Locate every uninfected red blood cell.
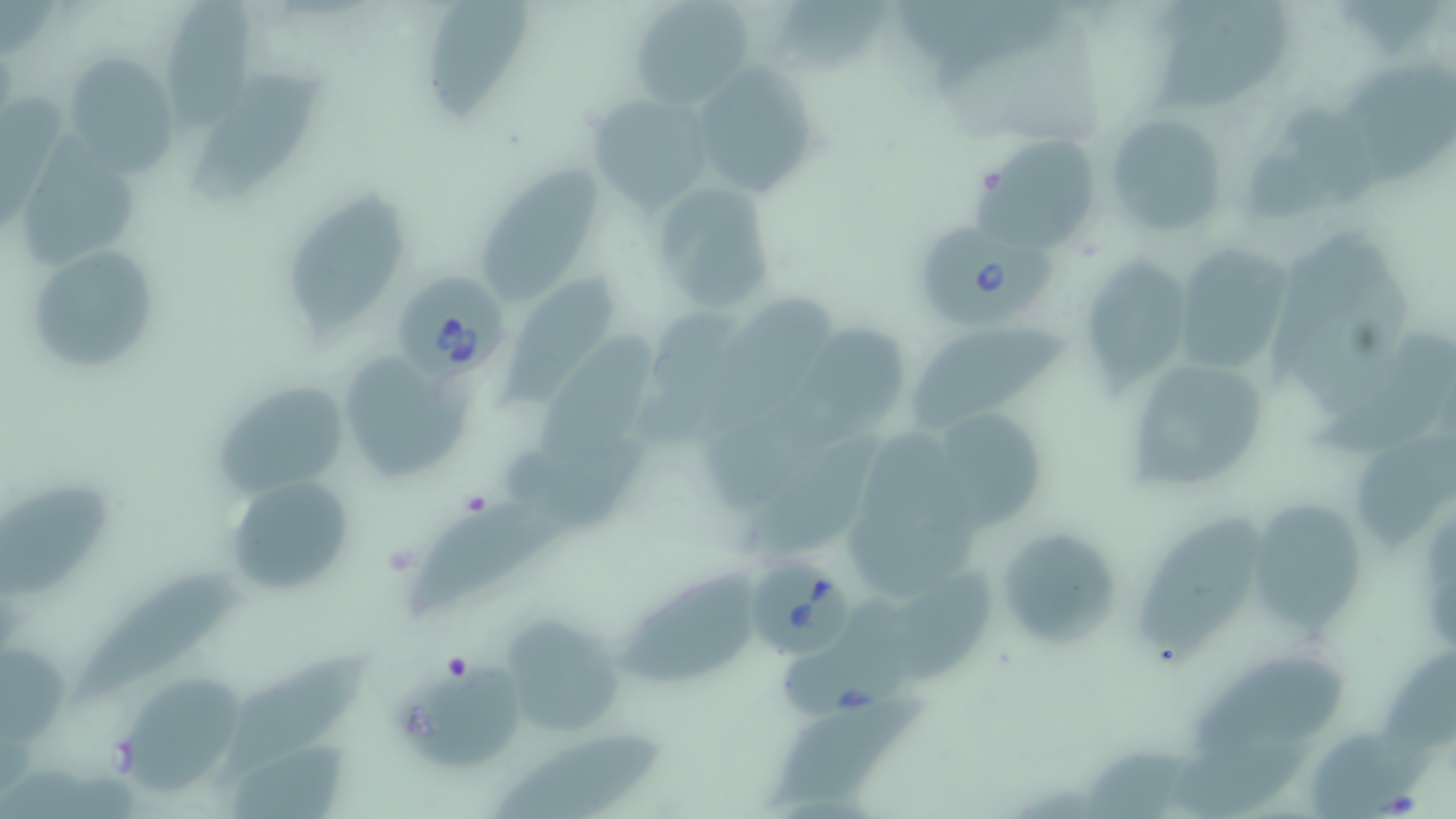
Approximate bounding boxes as (x1,y1)-(x2,y2) corner pairs in pixels.
Uninfected red blood cells: (167,0)-(255,130), (419,0)-(531,131), (627,0)-(756,108), (896,0)-(1066,78), (1160,5)-(1295,117), (63,55)-(180,174), (192,63)-(329,198), (690,64)-(814,197), (587,94)-(713,211), (1248,108)-(1378,225), (1103,112)-(1230,236), (26,132)-(144,267), (972,137)-(1096,241), (482,149)-(603,304), (647,179)-(776,318), (284,182)-(415,343), (22,242)-(161,375), (1180,249)-(1290,371), (1077,256)-(1193,393), (502,267)-(615,406), (701,296)-(841,437), (647,308)-(753,457), (536,327)-(660,465), (912,328)-(1069,429), (1321,334)-(1455,469), (344,350)-(479,480), (1119,353)-(1270,500), (209,378)-(352,503), (929,408)-(1049,528), (1355,427)-(1456,540), (492,436)-(657,528), (737,436)-(886,564), (223,475)-(354,597), (0,479)-(113,600), (414,500)-(570,618), (1262,501)-(1364,630), (1134,516)-(1265,658), (995,526)-(1126,650), (70,563)-(247,701), (623,567)-(751,689), (886,576)-(997,685), (497,611)-(628,738), (1,641)-(69,745), (224,644)-(368,782), (1377,646)-(1456,756), (396,649)-(524,774), (1192,659)-(1338,752), (133,677)-(244,800), (773,699)-(929,806), (494,730)-(666,819), (1164,732)-(1321,818).

Platelet locations: (462,491)-(489,517), (445,655)-(477,683). Babesia divergens-infected red blood cell locations: (921,219)-(1064,329), (396,265)-(512,382), (741,549)-(854,655). Slide-level diagnosis: Babesia divergens. Thin blood smear. One field of a larger specimen. 1000x magnification. Light microscopy. Image is 1456×819 pixels. May-Grünwald-Giemsa stain.